Report the malaria status of this cell.
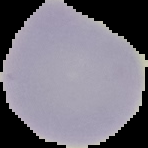

It is uninfected.

From a thin blood smear. Image is 148×148 pixels. Cell region segmented out of the field of view; the surrounding area is masked to black.